Outline each uninfected red blood cell.
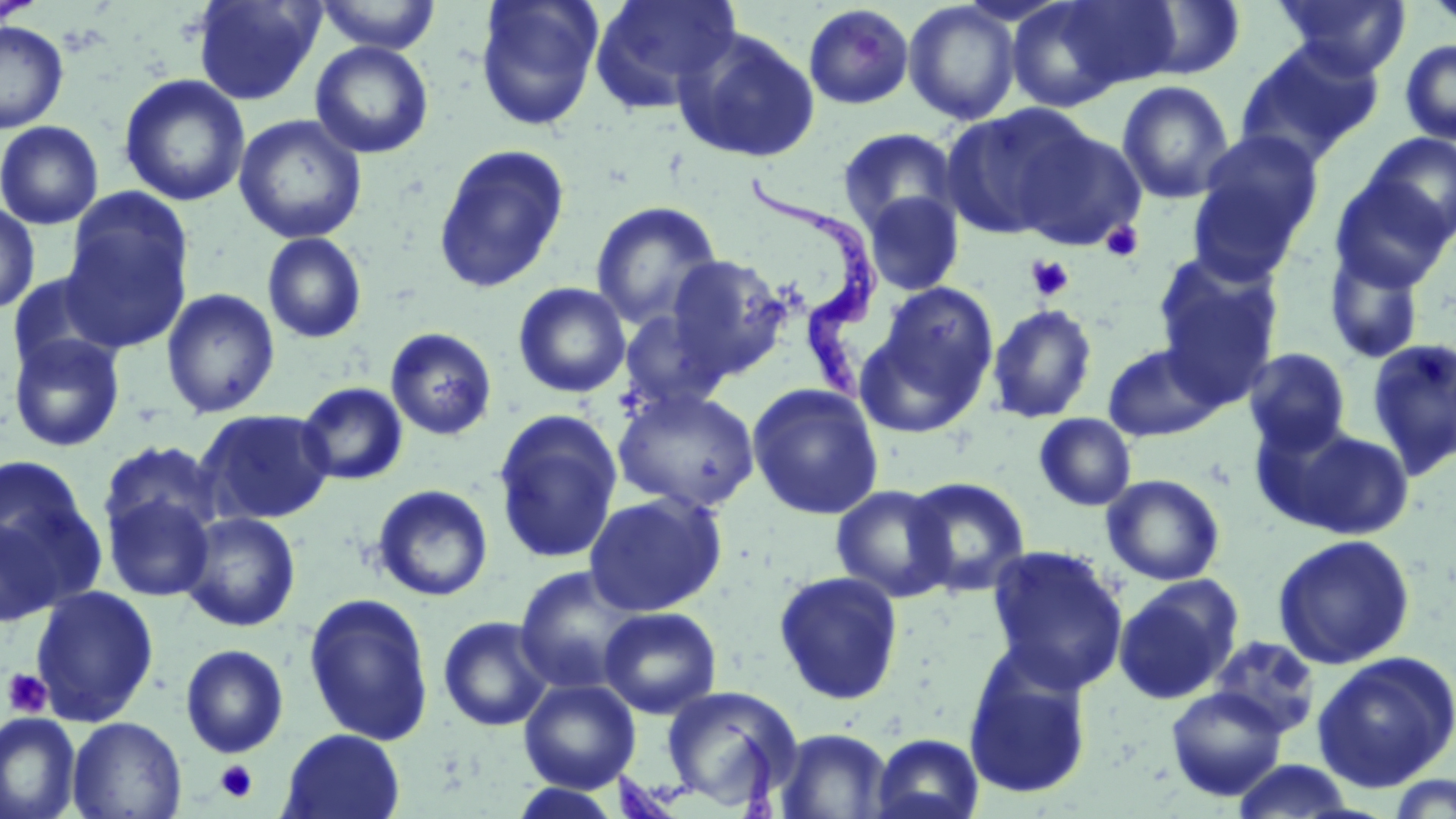

Approximate bounding boxes as [x1, y1, x2, y2] in pixels.
Uninfected red blood cells: [191, 0, 325, 105], [313, 0, 443, 54], [475, 0, 604, 131], [590, 0, 741, 112], [1006, 0, 1140, 112], [1049, 0, 1188, 93], [1273, 0, 1412, 78], [1420, 0, 1456, 32], [903, 1, 1021, 125], [1135, 2, 1247, 80], [803, 4, 915, 110], [0, 21, 69, 133], [672, 26, 821, 164], [1235, 39, 1385, 167], [1399, 39, 1456, 144], [310, 41, 434, 159], [119, 74, 250, 207], [1116, 80, 1235, 204], [941, 106, 1087, 240], [234, 114, 368, 244], [0, 120, 104, 229], [1012, 125, 1146, 250], [836, 127, 960, 236], [1194, 129, 1323, 259], [1362, 133, 1456, 245], [432, 143, 570, 294], [1329, 176, 1454, 291], [861, 190, 964, 296], [60, 198, 193, 351], [0, 200, 40, 315], [590, 200, 724, 330], [261, 232, 368, 344], [1324, 248, 1427, 365], [666, 255, 792, 379], [1153, 255, 1284, 406], [512, 281, 632, 398], [861, 283, 1000, 433], [161, 288, 280, 419], [986, 303, 1098, 423], [618, 310, 728, 413], [385, 327, 498, 440], [8, 332, 126, 453], [1366, 337, 1456, 477], [1102, 343, 1224, 441], [1243, 347, 1351, 453], [296, 382, 408, 486], [747, 383, 884, 520], [612, 387, 761, 513], [195, 408, 335, 525], [492, 409, 623, 565], [1034, 413, 1136, 511], [1264, 423, 1416, 540], [97, 440, 222, 545], [0, 456, 93, 569], [1102, 474, 1225, 586], [903, 476, 1031, 597], [372, 484, 493, 601], [830, 485, 956, 602], [102, 491, 215, 602], [583, 491, 728, 616], [180, 512, 301, 631], [0, 515, 65, 627], [1272, 533, 1416, 670], [985, 544, 1129, 693], [514, 565, 645, 694], [773, 570, 905, 706], [1113, 578, 1242, 705], [30, 585, 159, 726], [303, 592, 435, 746], [598, 606, 722, 719], [437, 616, 554, 732], [1207, 635, 1321, 740], [180, 644, 289, 759], [1311, 651, 1456, 792], [963, 653, 1094, 801], [519, 678, 641, 792], [660, 685, 803, 812], [1166, 687, 1288, 801], [0, 712, 82, 819], [67, 716, 187, 819], [773, 728, 894, 818], [279, 729, 405, 819], [871, 733, 984, 819], [1231, 759, 1358, 818], [1384, 775, 1456, 818], [507, 783, 626, 818].

Trypanosoma brucei locations: [743, 169, 882, 411], [616, 716, 786, 819]. Platelet locations: [1101, 221, 1144, 262], [1027, 256, 1074, 301], [2, 667, 52, 718], [215, 760, 258, 803]. Slide-level diagnosis: Trypanosoma brucei. May-Grünwald-Giemsa stain. Optical microscopy. Thin blood film. 1000x magnification. Image is 1456×819 pixels. Single field of view.